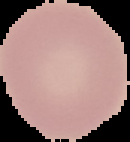

Result: no Plasmodium parasites detected. From a thin blood film. Image is 130×142 pixels. Cell region segmented out of the field of view; the surrounding area is masked to black.